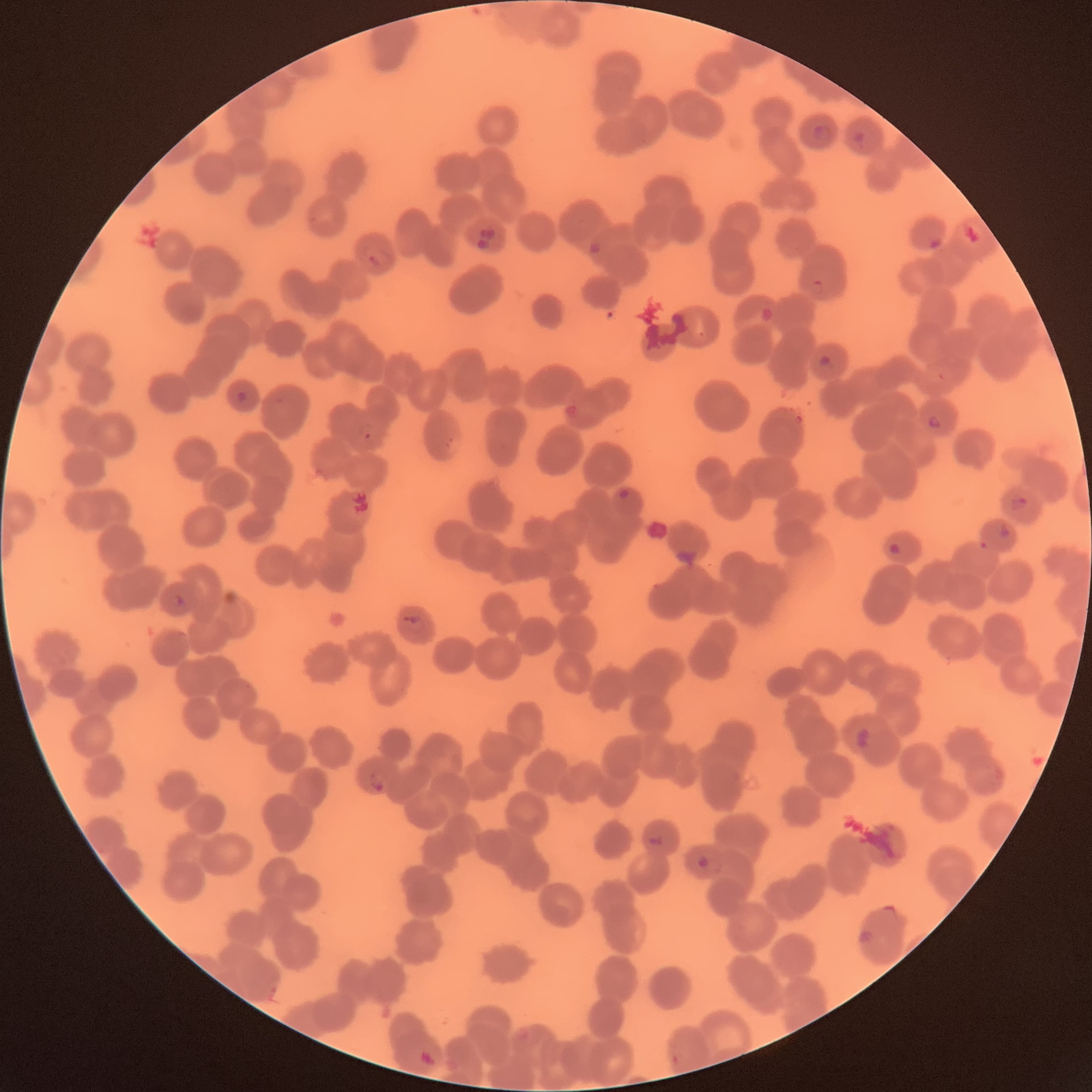

coordinate format = approximate bounding boxes as named x1/y1/x2/y2 corners in pixels
Plasmodium parasite locations = (x1=809, y1=124, x2=834, y2=142), (x1=854, y1=131, x2=865, y2=147), (x1=960, y1=221, x2=981, y2=245), (x1=587, y1=240, x2=604, y2=255), (x1=366, y1=244, x2=390, y2=266), (x1=809, y1=278, x2=825, y2=298), (x1=818, y1=355, x2=836, y2=369), (x1=235, y1=391, x2=249, y2=403), (x1=928, y1=415, x2=943, y2=430), (x1=357, y1=422, x2=374, y2=440), (x1=619, y1=489, x2=630, y2=499), (x1=1011, y1=497, x2=1028, y2=512), (x1=997, y1=521, x2=1012, y2=538), (x1=887, y1=543, x2=903, y2=555), (x1=174, y1=593, x2=187, y2=608), (x1=410, y1=616, x2=423, y2=631), (x1=367, y1=772, x2=386, y2=792), (x1=647, y1=835, x2=664, y2=846), (x1=697, y1=855, x2=722, y2=874), (x1=855, y1=930, x2=874, y2=944), (x1=420, y1=1048, x2=435, y2=1066), (x1=668, y1=1054, x2=681, y2=1065)
modality = light microscopy
image size = 1092×1092 pixels
preparation = thin blood smear
red blood cell morphology = rouleaux formation